Outline each blood parasite and name the species.
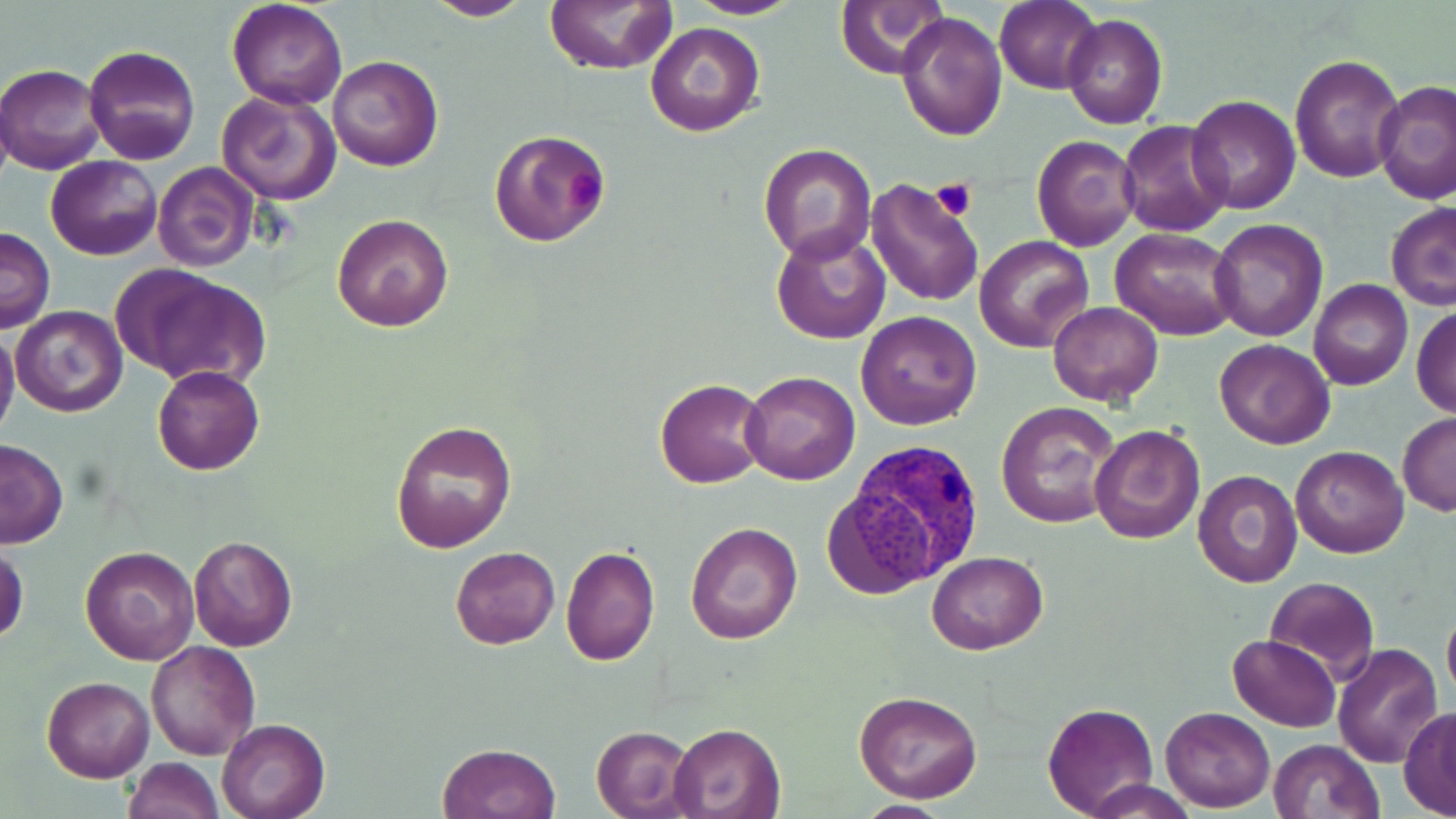
Approximate bounding boxes as (x1,y1)-(x2,y2) corner pairs in pixels.
Plasmodium vivax-infected red blood cells: (831,442)-(985,593).
No Plasmodium falciparum, Plasmodium ovale, Plasmodium malariae, Babesia divergens, or Trypanosoma brucei observed.

Uninfected red blood cell locations: (420,0)-(533,22), (685,0)-(803,19), (837,0)-(951,79), (226,1)-(348,111), (544,1)-(675,75), (995,1)-(1101,92), (896,10)-(1007,143), (1063,13)-(1168,129), (643,21)-(765,136), (83,45)-(199,166), (1290,53)-(1402,182), (328,56)-(444,172), (1,63)-(106,173), (1372,80)-(1456,206), (215,89)-(341,205), (1187,95)-(1301,215), (1119,121)-(1233,236), (489,128)-(611,247), (1031,135)-(1139,251), (757,141)-(878,265), (45,155)-(161,260), (153,160)-(259,272), (864,175)-(986,308), (1386,201)-(1456,310), (332,213)-(454,332), (1209,218)-(1327,340), (771,226)-(892,346), (0,227)-(55,331), (1110,228)-(1241,341), (977,235)-(1093,353), (118,266)-(267,388), (1308,279)-(1412,391), (1046,301)-(1164,406), (11,304)-(127,418), (1411,305)-(1456,418), (855,310)-(983,429), (0,328)-(20,444), (1215,339)-(1335,449), (152,365)-(265,476), (739,371)-(860,485), (654,377)-(769,489), (995,402)-(1120,528), (1397,412)-(1456,518), (391,420)-(517,552), (1089,424)-(1206,544), (0,441)-(68,548), (1291,445)-(1410,558), (1192,470)-(1301,588), (684,521)-(802,646), (187,535)-(298,654), (0,542)-(28,645), (80,544)-(200,665), (450,545)-(559,648), (560,545)-(659,666), (926,551)-(1049,656), (1264,577)-(1380,682), (1442,600)-(1456,710), (1228,634)-(1341,731), (146,640)-(260,759), (1332,642)-(1445,769), (42,676)-(154,783), (853,690)-(983,804), (1042,702)-(1158,817), (1160,706)-(1275,812), (1399,707)-(1456,818), (217,718)-(330,819), (667,723)-(786,818), (591,725)-(696,818), (1268,738)-(1382,819), (439,743)-(562,819), (123,756)-(224,819), (1084,779)-(1196,819), (853,800)-(956,819). Platelet locations: (558,167)-(603,211), (932,179)-(977,222). Slide-level diagnosis: Plasmodium vivax. Thin blood film. Single field of view. Optical microscopy. May-Grünwald-Giemsa-stained preparation. Image is 1456×819 pixels. 1000x magnification.